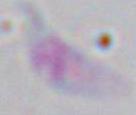

Summary:
  - Modality: photomicrograph
  - Identification: Toxoplasma gondii
  - Magnification: 1000x